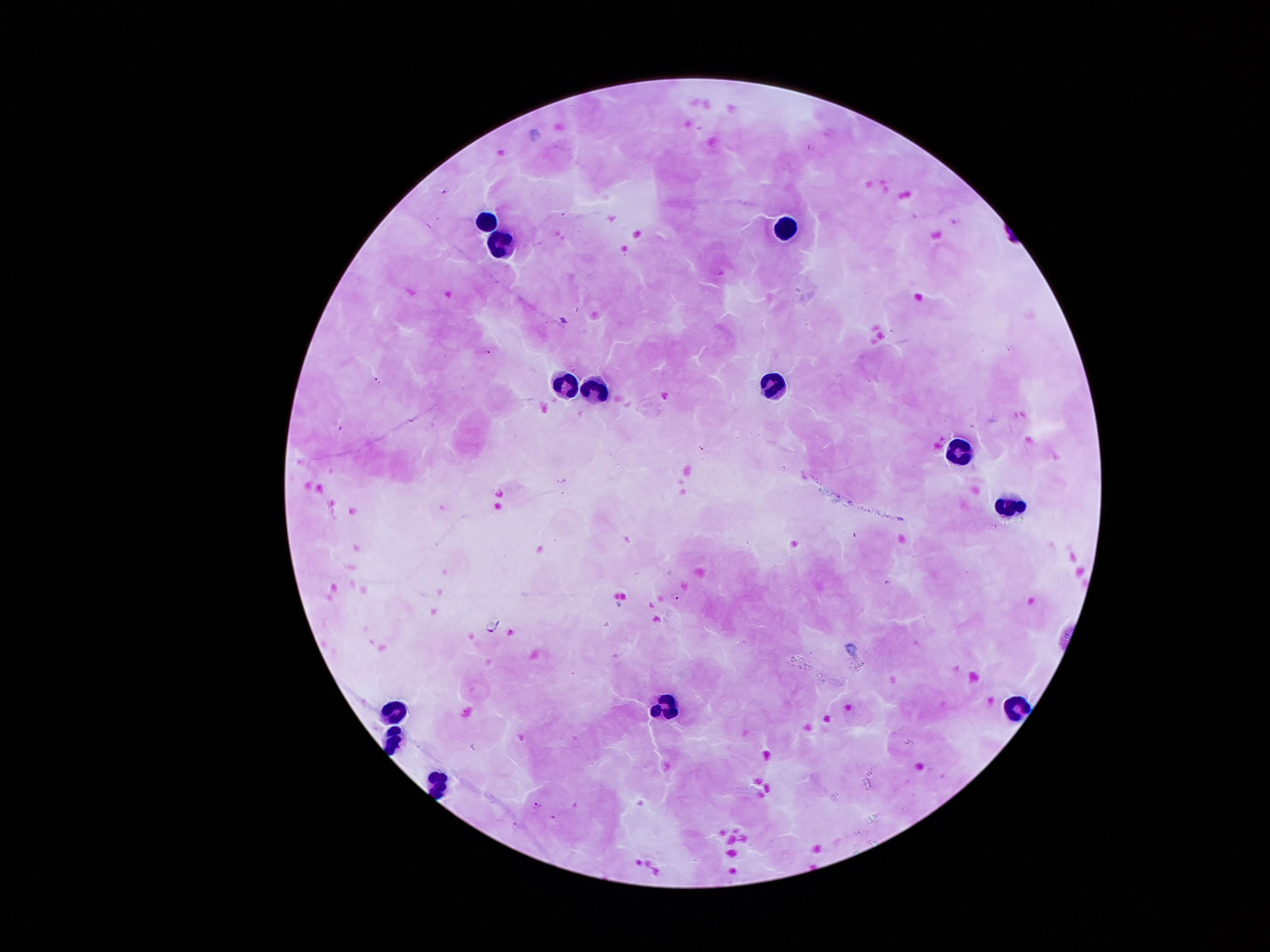

Approximate object centers, in pixels from the top-left corner. Malaria parasite locations: (x=488, y=352), (x=377, y=380), (x=341, y=428), (x=563, y=482), (x=678, y=597), (x=537, y=804), (x=554, y=818). Leukocyte locations: (x=483, y=220), (x=783, y=227), (x=497, y=242), (x=771, y=379), (x=571, y=380), (x=595, y=388), (x=956, y=451), (x=1011, y=498), (x=392, y=701), (x=664, y=702), (x=1016, y=704), (x=390, y=736), (x=439, y=781). 100x magnification. Thick blood smear. Single field of view. Patient malaria status: infected with Plasmodium falciparum. Photographed through the microscope eyepiece with a smartphone camera. Giemsa stain. Image is 1270×952 pixels.